Identify the blood parasite species.
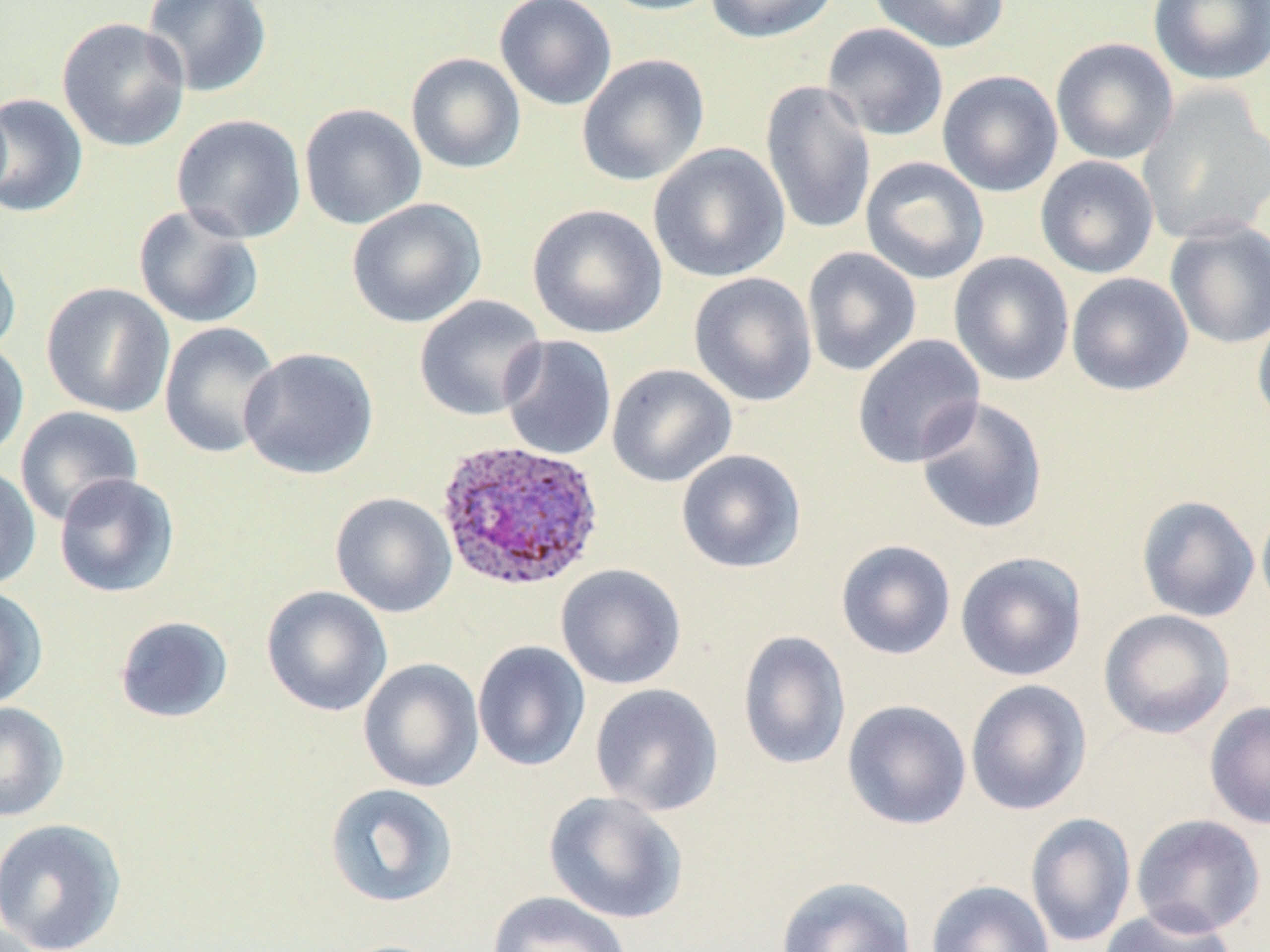
Plasmodium ovale.

field of view = single
magnification = 1000x
image size = 1270×952 pixels
Plasmodium ovale-infected red blood cell locations = approximate bounding boxes as (x1, y1, x2, y2) in pixels: (436, 438, 605, 592)
uninfected red blood cell locations = approximate bounding boxes as (x1, y1, x2, y2) in pixels: (141, 0, 273, 99), (494, 0, 617, 110), (597, 0, 727, 16), (705, 0, 840, 44), (868, 0, 1009, 53), (1148, 0, 1270, 86), (56, 17, 191, 153), (821, 22, 949, 142), (1050, 37, 1179, 165), (405, 52, 526, 174), (576, 54, 709, 187), (937, 70, 1063, 197), (759, 79, 877, 238), (1137, 87, 1270, 245), (0, 93, 89, 218), (299, 103, 427, 230), (171, 114, 307, 244), (648, 142, 790, 283), (1035, 155, 1159, 279), (860, 156, 989, 284), (347, 198, 487, 329), (527, 203, 667, 339), (132, 204, 264, 329), (1164, 217, 1270, 349), (0, 241, 22, 359), (801, 247, 922, 377), (948, 251, 1075, 387), (688, 271, 818, 407), (1066, 272, 1193, 396), (41, 282, 176, 418), (414, 295, 547, 422), (1252, 308, 1270, 433), (158, 321, 281, 458), (499, 334, 617, 460), (851, 334, 986, 469), (0, 337, 29, 463), (238, 347, 379, 480), (606, 363, 737, 487), (914, 396, 1049, 535), (14, 405, 144, 526), (676, 449, 806, 574), (0, 463, 41, 591), (53, 473, 180, 598), (330, 492, 457, 618), (1136, 494, 1260, 623), (1256, 496, 1270, 619), (835, 539, 956, 660), (955, 551, 1087, 682), (556, 563, 686, 690), (0, 585, 48, 710), (261, 585, 393, 717), (1098, 609, 1236, 739), (114, 615, 234, 724), (738, 630, 851, 770), (472, 640, 591, 772), (358, 658, 484, 793), (965, 678, 1092, 816), (590, 683, 724, 815), (842, 699, 972, 830), (1204, 700, 1270, 830), (0, 702, 69, 822), (324, 782, 459, 909), (542, 791, 689, 925), (1025, 812, 1136, 948), (1131, 813, 1266, 938), (0, 817, 128, 952), (775, 876, 918, 952), (926, 879, 1055, 952), (486, 890, 634, 952), (1097, 905, 1236, 952)
stain = May-Grünwald-Giemsa
preparation = thin blood smear
modality = light microscopy